Locate and identify every blood parasite.
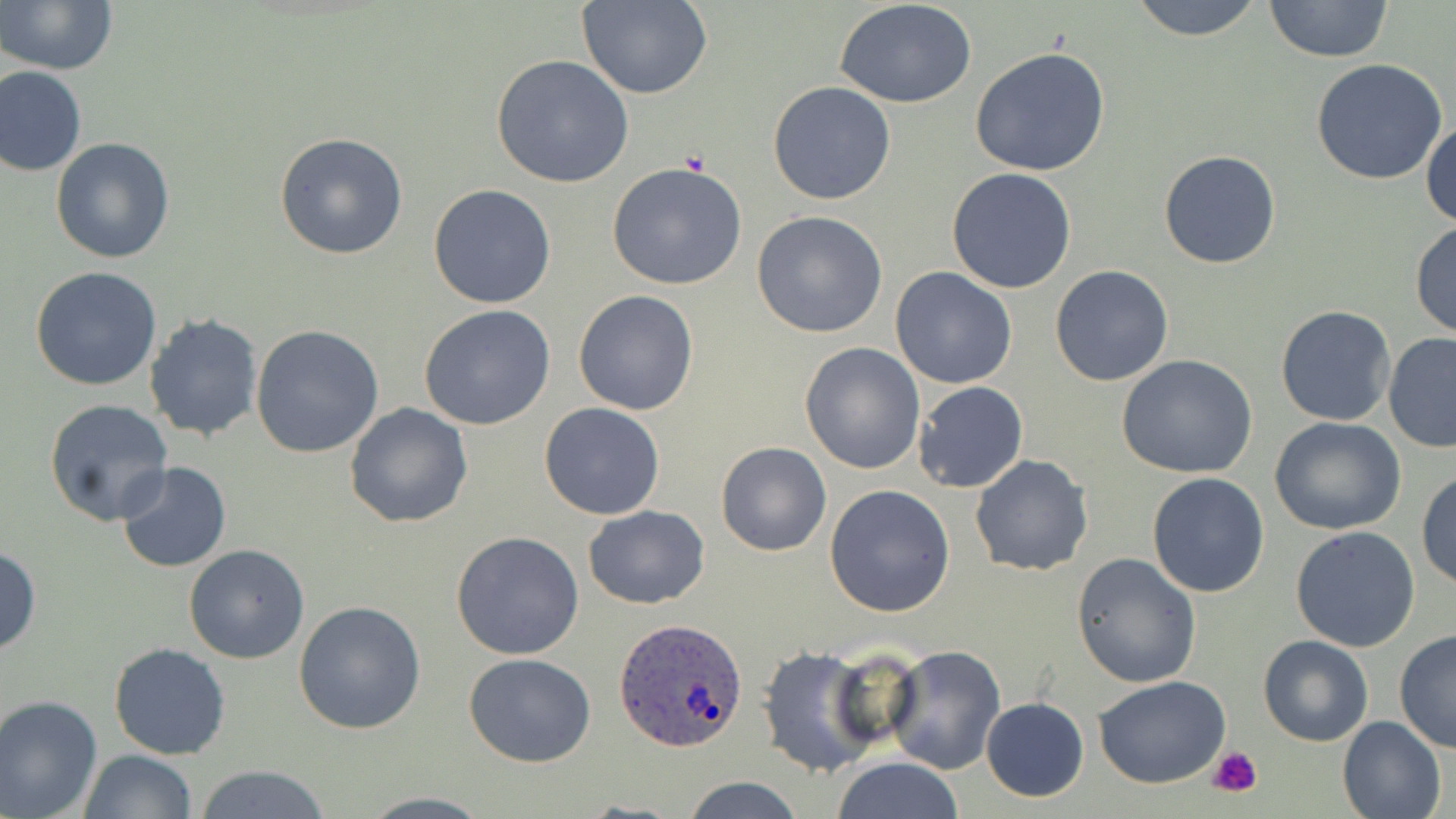
Approximate bounding boxes as (x1, y1, x2, y2) in pixels.
Plasmodium ovale-infected red blood cells: (614, 618, 748, 755).
No Plasmodium falciparum, Plasmodium malariae, Plasmodium vivax, Babesia divergens, or Trypanosoma brucei observed.

slide-level diagnosis = Plasmodium ovale
stain = May-Grünwald-Giemsa
image size = 1456×819 pixels
uninfected red blood cell locations = approximate bounding boxes as (x1, y1, x2, y2) in pixels: (576, 0, 713, 100), (1127, 0, 1266, 42), (1263, 0, 1393, 62), (2, 1, 119, 75), (835, 1, 979, 108), (969, 46, 1112, 177), (491, 54, 634, 188), (1310, 58, 1449, 187), (0, 66, 86, 177), (767, 81, 897, 205), (1421, 118, 1455, 227), (273, 131, 408, 260), (51, 136, 176, 263), (1158, 150, 1281, 270), (606, 163, 747, 290), (946, 168, 1077, 294), (428, 184, 557, 309), (752, 210, 890, 339), (1410, 220, 1456, 340), (31, 265, 163, 391), (1050, 265, 1175, 387), (891, 267, 1017, 389), (574, 290, 698, 416), (1274, 304, 1394, 427), (419, 305, 556, 430), (145, 313, 263, 441), (251, 326, 384, 460), (1382, 332, 1456, 453), (799, 342, 926, 474), (1117, 355, 1260, 479), (913, 381, 1029, 494), (44, 398, 174, 526), (539, 401, 666, 521), (345, 403, 473, 529), (1270, 416, 1407, 535), (716, 441, 831, 556), (969, 455, 1093, 576), (116, 461, 232, 573), (1416, 471, 1456, 590), (1147, 473, 1271, 596), (824, 484, 956, 616), (583, 506, 710, 608), (1290, 524, 1422, 651), (451, 531, 585, 661), (0, 544, 41, 655), (183, 545, 311, 664), (1072, 552, 1201, 687), (293, 601, 426, 734), (1394, 630, 1455, 753), (1258, 634, 1373, 746), (108, 642, 231, 759), (756, 644, 880, 778), (882, 644, 1006, 775), (464, 653, 596, 767), (1093, 676, 1230, 789), (0, 694, 103, 817), (980, 698, 1088, 802), (1337, 715, 1448, 819), (78, 749, 195, 819), (830, 757, 965, 818), (195, 764, 330, 819), (680, 775, 806, 818), (356, 792, 495, 818)
platelet locations = approximate bounding boxes as (x1, y1, x2, y2) in pixels: (1209, 746, 1263, 796)
preparation = thin blood smear
field of view = one of a larger specimen
magnification = 1000x
modality = light microscopy